Identify the blood parasite species.
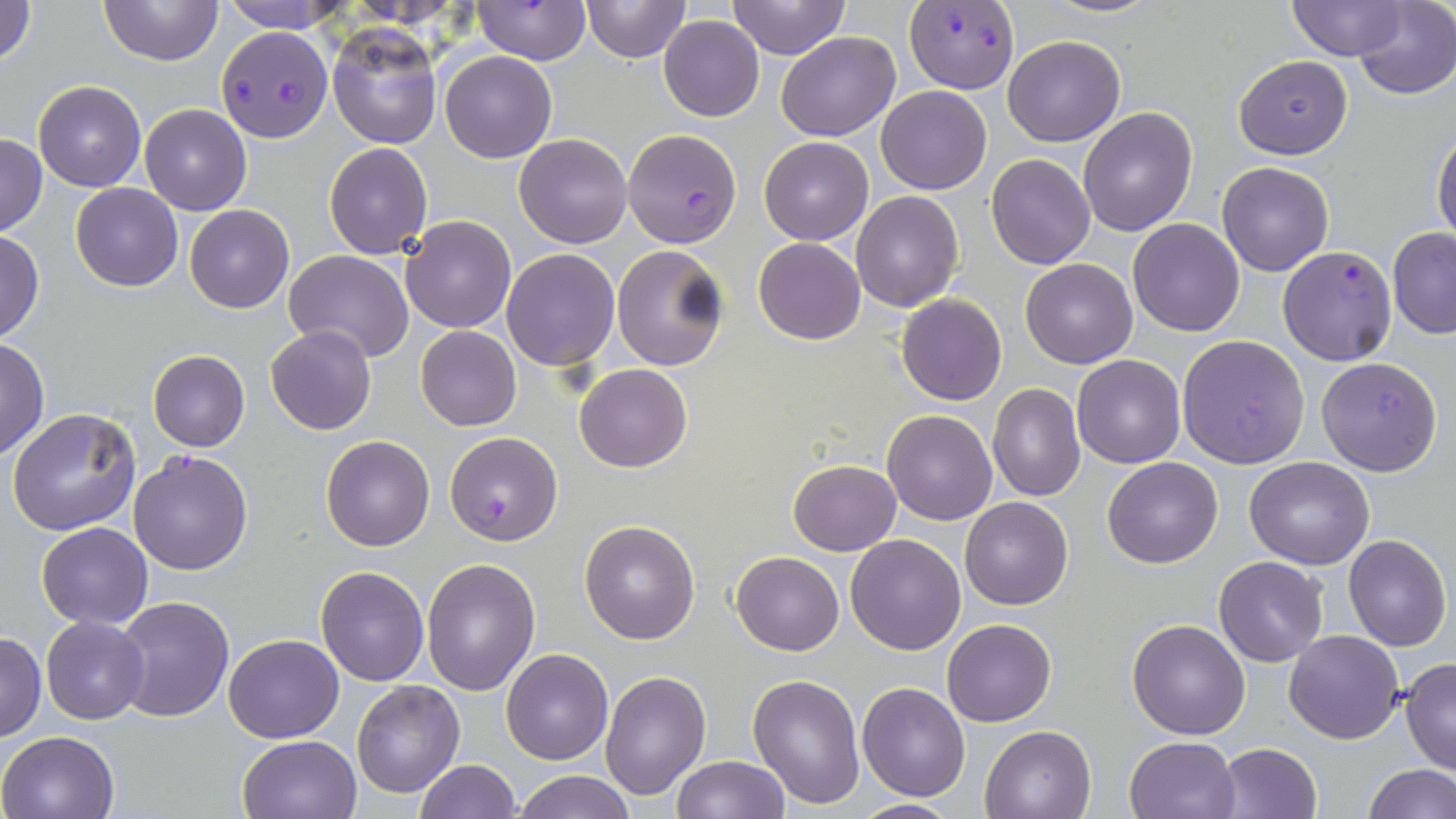
Plasmodium falciparum.

Summary:
  - Coordinate format: approximate bounding boxes as (x1, y1, x2, y2) in pixels
  - Uninfected red blood cell locations: (0, 0, 38, 66), (98, 0, 221, 67), (218, 0, 349, 32), (582, 0, 688, 62), (727, 0, 851, 60), (1041, 0, 1161, 19), (1288, 0, 1403, 60), (1351, 0, 1455, 100), (475, 1, 588, 63), (659, 14, 764, 121), (328, 25, 442, 149), (776, 30, 899, 141), (1003, 34, 1125, 147), (440, 50, 557, 162), (1234, 55, 1352, 159), (33, 80, 145, 191), (877, 86, 992, 195), (139, 103, 251, 215), (1078, 106, 1197, 235), (1432, 128, 1455, 246), (0, 134, 47, 235), (514, 134, 632, 248), (759, 137, 873, 244), (324, 143, 432, 258), (986, 154, 1096, 270), (1217, 162, 1334, 276), (70, 183, 182, 291), (851, 190, 964, 312), (184, 204, 294, 313), (400, 215, 517, 332), (1127, 219, 1246, 336), (1387, 228, 1456, 339), (0, 231, 44, 341), (753, 237, 866, 345), (611, 244, 730, 371), (501, 249, 619, 369), (283, 250, 415, 363), (1020, 258, 1138, 369), (896, 294, 1006, 405), (266, 325, 377, 435), (415, 325, 522, 431), (1177, 334, 1311, 469), (0, 338, 49, 459), (148, 351, 250, 451), (1073, 355, 1185, 469), (1316, 355, 1443, 475), (574, 363, 692, 472), (987, 383, 1086, 502), (8, 407, 142, 536), (882, 410, 998, 525), (320, 435, 434, 550), (1244, 457, 1374, 569), (1101, 458, 1221, 568), (789, 459, 901, 555), (959, 496, 1073, 610), (580, 519, 702, 644), (37, 521, 153, 629), (845, 533, 966, 655), (1343, 535, 1452, 652), (730, 551, 844, 656), (1213, 556, 1329, 666), (422, 557, 540, 694), (316, 565, 430, 685), (113, 596, 233, 722), (40, 615, 149, 724), (942, 618, 1057, 726), (1127, 618, 1251, 738), (1284, 629, 1404, 744), (1, 632, 46, 741), (225, 634, 345, 742), (501, 648, 613, 765), (1399, 658, 1456, 774), (599, 668, 712, 801), (748, 674, 865, 810), (352, 680, 465, 799), (857, 681, 972, 801), (979, 725, 1096, 819), (0, 730, 119, 818), (238, 734, 363, 819), (1125, 735, 1239, 819), (1216, 742, 1323, 819), (670, 756, 790, 818), (416, 759, 521, 818), (1362, 764, 1455, 819), (513, 770, 636, 819), (847, 798, 963, 817)
  - Plasmodium falciparum-infected red blood cell locations: (904, 3, 1019, 95), (218, 27, 333, 142), (624, 129, 741, 247), (1278, 246, 1398, 365), (446, 431, 563, 546), (128, 450, 252, 575)
  - Image size: 1456×819 pixels
  - Magnification: 1000x
  - Stain: May-Grünwald-Giemsa
  - Preparation: thin blood film
  - Modality: optical microscopy
  - Field of view: single